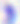
modality: photomicrograph
magnification: 400x
identification: Toxoplasma gondii